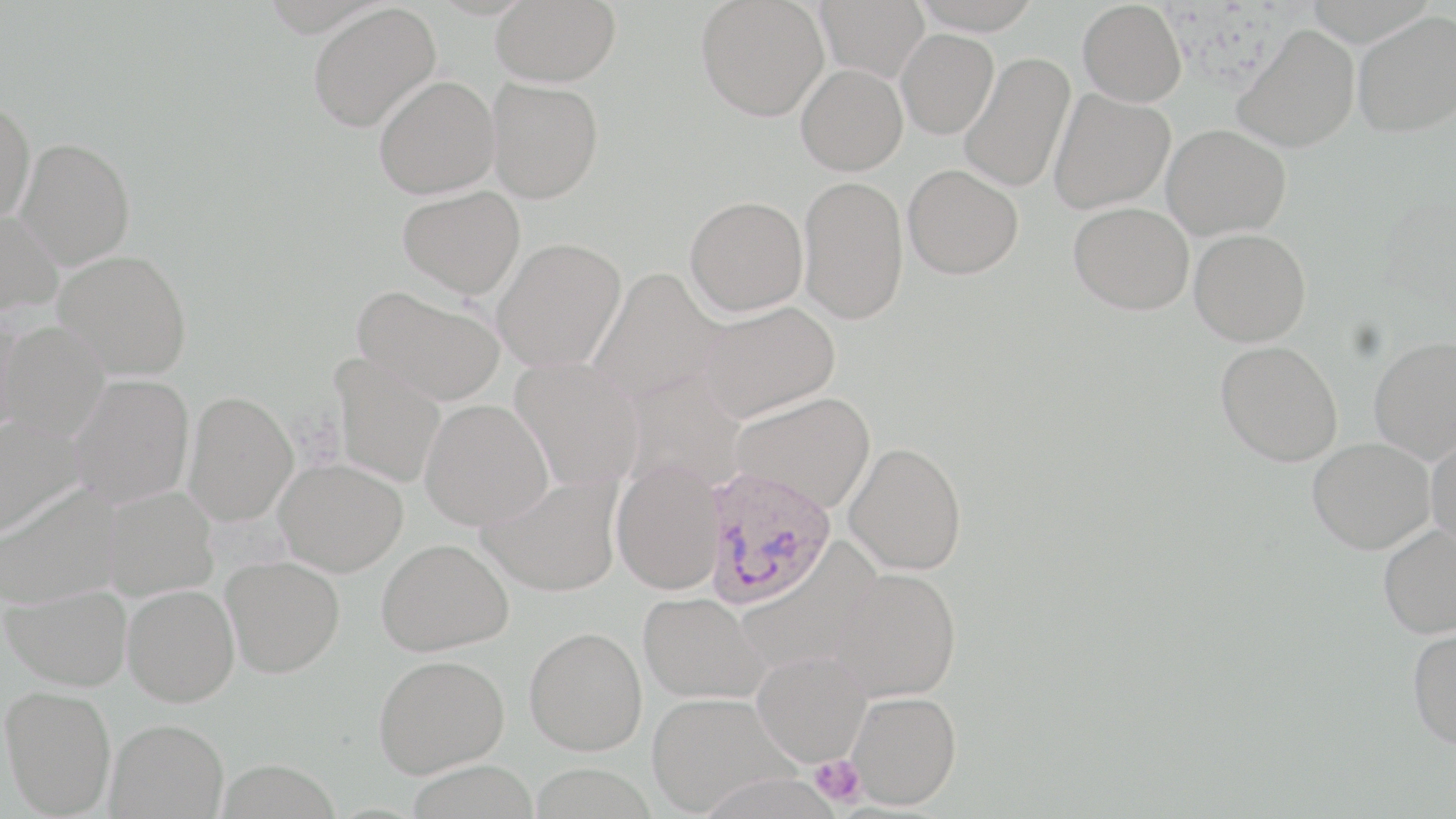
{
  "slide_level_diagnosis": "Plasmodium ovale",
  "uninfected_red_blood_cell_locations": "approximate bounding boxes as [x1, y1, x2, y2] in pixels: [491, 0, 621, 87], [696, 0, 830, 121], [814, 0, 930, 82], [911, 0, 1044, 35], [1077, 1, 1187, 107], [308, 2, 441, 133], [1353, 11, 1455, 138], [1233, 24, 1360, 153], [896, 28, 999, 139], [959, 52, 1075, 193], [796, 64, 907, 175], [373, 75, 501, 199], [486, 78, 604, 202], [1048, 89, 1175, 214], [0, 99, 35, 227], [1161, 125, 1291, 240], [15, 137, 136, 269], [903, 164, 1023, 279], [798, 175, 909, 325], [397, 185, 526, 298], [685, 195, 808, 316], [1069, 202, 1194, 315], [0, 210, 63, 316], [1189, 228, 1311, 346], [491, 237, 627, 372], [53, 249, 192, 381], [588, 268, 725, 408], [353, 285, 506, 406], [698, 300, 839, 422], [0, 309, 26, 440], [1, 322, 110, 443], [1368, 336, 1456, 463], [1216, 341, 1343, 466], [329, 354, 447, 488], [510, 357, 645, 493], [68, 374, 194, 508], [183, 390, 298, 526], [730, 391, 876, 513], [420, 399, 553, 530], [0, 416, 84, 538], [1426, 432, 1456, 550], [1308, 437, 1435, 553], [844, 442, 967, 575], [274, 458, 408, 576], [612, 458, 725, 595], [478, 472, 623, 597], [0, 483, 128, 609], [96, 485, 218, 601], [1377, 524, 1456, 638], [376, 538, 514, 656], [222, 557, 344, 677], [830, 567, 962, 703], [3, 582, 132, 692], [122, 583, 240, 706], [638, 591, 769, 704], [525, 626, 648, 755], [1407, 626, 1456, 750], [752, 650, 871, 766], [374, 653, 510, 778], [1, 685, 117, 816], [847, 690, 961, 809], [648, 691, 796, 815], [105, 718, 228, 818]",
  "image_size": "1456×819 pixels",
  "field_of_view": "single",
  "platelet_locations": "approximate bounding boxes as [x1, y1, x2, y2] in pixels: [810, 754, 864, 806]",
  "plasmodium_ovale_infected_red_blood_cell_locations": "approximate bounding boxes as [x1, y1, x2, y2] in pixels: [701, 466, 839, 609]",
  "magnification": "1000x",
  "preparation": "thin blood smear",
  "modality": "light microscopy",
  "stain": "May-Grünwald-Giemsa"
}